Assess the morphology of the red blood cells.
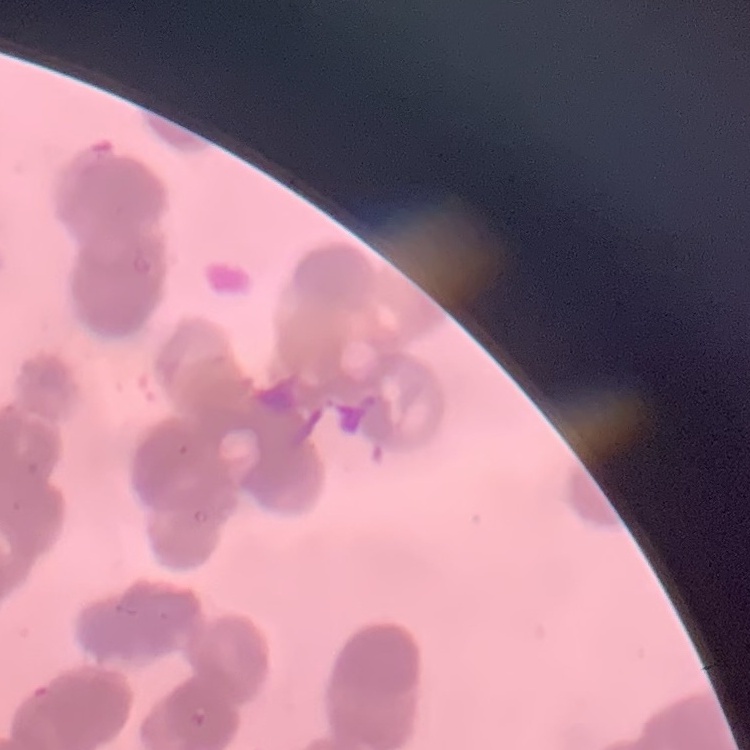
They show rouleaux formation.

Summary:
  - Preparation: thin blood film
  - Image type: one tile cut from a larger photomicrograph
  - Stain: Field's or Giemsa